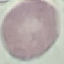

{
  "result": "no malaria parasites detected",
  "image_type": "automatically extracted cell patch, resized to 64 × 64 pixels",
  "capture": "smartphone through the microscope eyepiece",
  "preparation": "thin blood smear",
  "stain": "Giemsa"
}